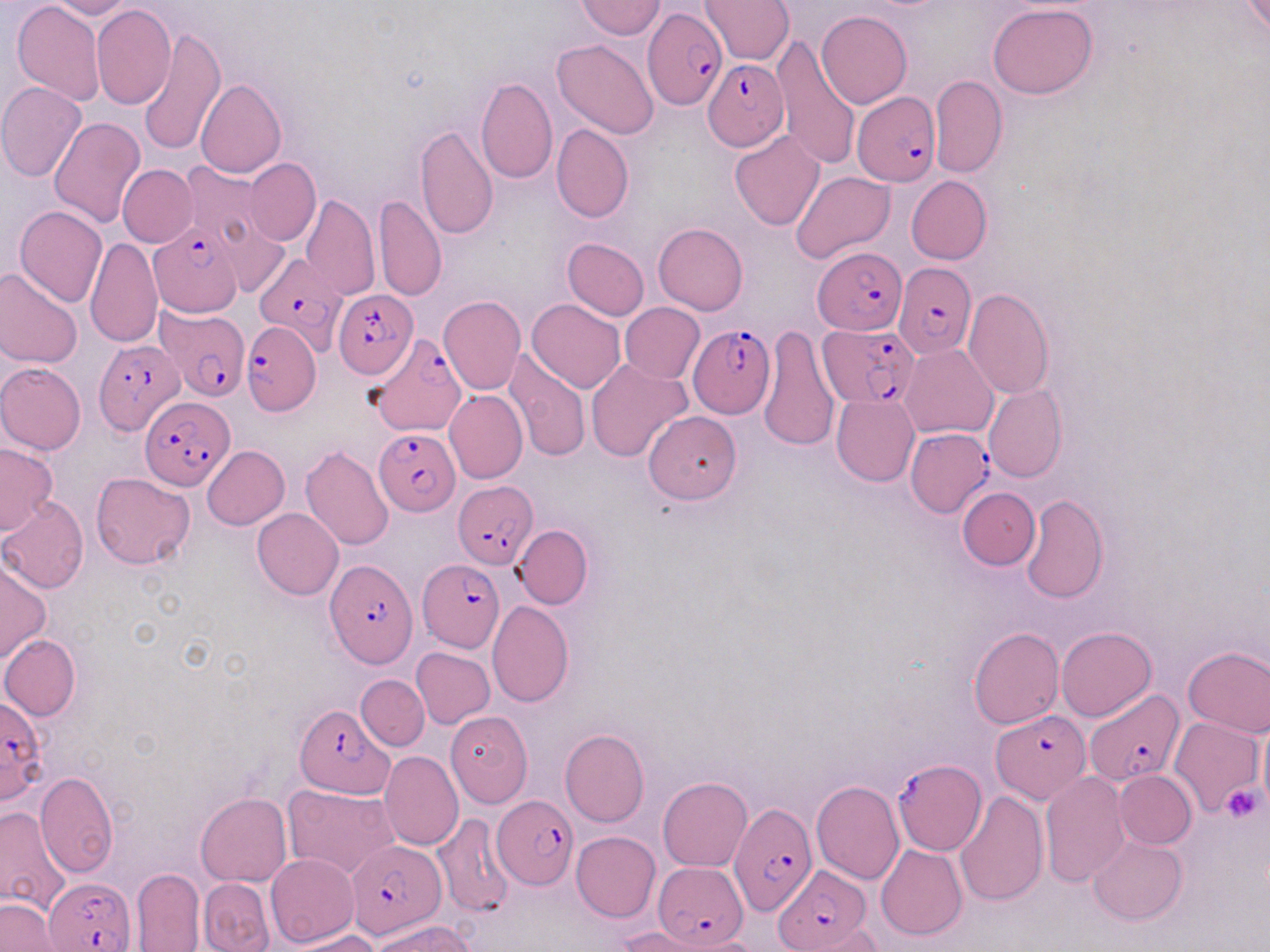

Summary:
  - Coordinate format: approximate bounding boxes as named x1/y1/x2/y2 corners in pixels
  - Plasmodium falciparum-infected red blood cell locations: (x1=640, y1=4, x2=725, y2=112), (x1=702, y1=59, x2=789, y2=150), (x1=852, y1=91, x2=941, y2=186), (x1=149, y1=219, x2=248, y2=321), (x1=815, y1=246, x2=908, y2=336), (x1=255, y1=249, x2=349, y2=354), (x1=892, y1=263, x2=975, y2=358), (x1=335, y1=291, x2=416, y2=376), (x1=156, y1=307, x2=250, y2=399), (x1=241, y1=318, x2=320, y2=416), (x1=689, y1=322, x2=776, y2=418), (x1=819, y1=324, x2=918, y2=406), (x1=365, y1=331, x2=465, y2=440), (x1=94, y1=338, x2=184, y2=434), (x1=140, y1=396, x2=234, y2=489), (x1=904, y1=426, x2=991, y2=517), (x1=374, y1=429, x2=458, y2=514), (x1=453, y1=481, x2=537, y2=568), (x1=418, y1=559, x2=505, y2=653), (x1=325, y1=561, x2=415, y2=666), (x1=1085, y1=691, x2=1184, y2=785), (x1=1, y1=696, x2=49, y2=805), (x1=293, y1=704, x2=391, y2=797), (x1=991, y1=708, x2=1088, y2=803), (x1=892, y1=760, x2=985, y2=854), (x1=492, y1=797, x2=576, y2=890), (x1=730, y1=802, x2=817, y2=921), (x1=346, y1=839, x2=444, y2=938), (x1=652, y1=862, x2=749, y2=948), (x1=771, y1=868, x2=870, y2=949), (x1=45, y1=877, x2=136, y2=952)
  - Platelet locations: (x1=1221, y1=784, x2=1265, y2=824)
  - Uninfected red blood cell locations: (x1=11, y1=0, x2=105, y2=106), (x1=45, y1=0, x2=135, y2=19), (x1=700, y1=0, x2=794, y2=65), (x1=575, y1=1, x2=666, y2=40), (x1=92, y1=5, x2=175, y2=110), (x1=989, y1=5, x2=1098, y2=98), (x1=817, y1=10, x2=912, y2=109), (x1=138, y1=28, x2=226, y2=156), (x1=772, y1=35, x2=861, y2=170), (x1=553, y1=40, x2=660, y2=140), (x1=929, y1=74, x2=1007, y2=178), (x1=476, y1=78, x2=557, y2=184), (x1=195, y1=80, x2=287, y2=178), (x1=0, y1=83, x2=87, y2=182), (x1=49, y1=116, x2=146, y2=227), (x1=415, y1=123, x2=499, y2=240), (x1=552, y1=123, x2=633, y2=223), (x1=730, y1=131, x2=826, y2=230), (x1=244, y1=159, x2=320, y2=245), (x1=177, y1=160, x2=276, y2=253), (x1=118, y1=166, x2=196, y2=246), (x1=790, y1=171, x2=896, y2=265), (x1=906, y1=175, x2=991, y2=264), (x1=374, y1=193, x2=446, y2=302), (x1=301, y1=194, x2=380, y2=302), (x1=15, y1=206, x2=108, y2=308), (x1=653, y1=223, x2=748, y2=314), (x1=85, y1=236, x2=161, y2=349), (x1=562, y1=238, x2=649, y2=319), (x1=0, y1=267, x2=83, y2=369), (x1=962, y1=288, x2=1055, y2=401), (x1=439, y1=295, x2=525, y2=395), (x1=528, y1=299, x2=626, y2=392), (x1=620, y1=303, x2=704, y2=384), (x1=757, y1=327, x2=841, y2=452), (x1=901, y1=344, x2=997, y2=439), (x1=504, y1=350, x2=590, y2=463), (x1=585, y1=359, x2=692, y2=462), (x1=0, y1=363, x2=86, y2=454), (x1=983, y1=385, x2=1067, y2=482), (x1=445, y1=390, x2=528, y2=483), (x1=831, y1=394, x2=919, y2=486), (x1=644, y1=411, x2=742, y2=503), (x1=0, y1=443, x2=57, y2=536), (x1=202, y1=445, x2=289, y2=530), (x1=300, y1=446, x2=393, y2=550), (x1=91, y1=471, x2=196, y2=569), (x1=957, y1=488, x2=1039, y2=569), (x1=1021, y1=494, x2=1108, y2=601), (x1=0, y1=498, x2=88, y2=593), (x1=252, y1=508, x2=343, y2=599), (x1=512, y1=525, x2=593, y2=609), (x1=0, y1=560, x2=50, y2=663), (x1=487, y1=601, x2=573, y2=707), (x1=1056, y1=626, x2=1156, y2=721), (x1=969, y1=627, x2=1064, y2=729), (x1=1, y1=634, x2=81, y2=720), (x1=1183, y1=646, x2=1270, y2=738), (x1=411, y1=647, x2=494, y2=729), (x1=356, y1=675, x2=429, y2=750), (x1=445, y1=711, x2=532, y2=808), (x1=1257, y1=715, x2=1270, y2=817), (x1=1169, y1=716, x2=1263, y2=817), (x1=559, y1=729, x2=649, y2=827), (x1=379, y1=750, x2=464, y2=850), (x1=1114, y1=771, x2=1195, y2=849), (x1=36, y1=772, x2=118, y2=876), (x1=1040, y1=772, x2=1131, y2=888), (x1=658, y1=777, x2=752, y2=871), (x1=812, y1=780, x2=904, y2=884), (x1=282, y1=784, x2=399, y2=879), (x1=956, y1=791, x2=1048, y2=906), (x1=195, y1=792, x2=291, y2=886), (x1=0, y1=807, x2=70, y2=919), (x1=428, y1=812, x2=518, y2=918), (x1=572, y1=831, x2=660, y2=921), (x1=1088, y1=834, x2=1187, y2=926), (x1=876, y1=844, x2=968, y2=940), (x1=265, y1=853, x2=359, y2=948), (x1=132, y1=868, x2=206, y2=951), (x1=197, y1=878, x2=275, y2=952), (x1=0, y1=897, x2=62, y2=952), (x1=370, y1=918, x2=477, y2=952), (x1=615, y1=925, x2=730, y2=952), (x1=291, y1=930, x2=380, y2=952)
  - Slide-level diagnosis: Plasmodium falciparum
  - Preparation: thin blood smear
  - Modality: light microscopy
  - Field of view: one of a larger specimen
  - Image size: 1270×952 pixels
  - Magnification: 1000x
  - Stain: May-Grünwald-Giemsa